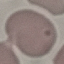

result = no malaria parasites seen
capture = smartphone camera at the microscope eyepiece
preparation = thin blood film
stain = Giemsa
image type = automatically extracted cell patch, resized to 64 × 64 pixels